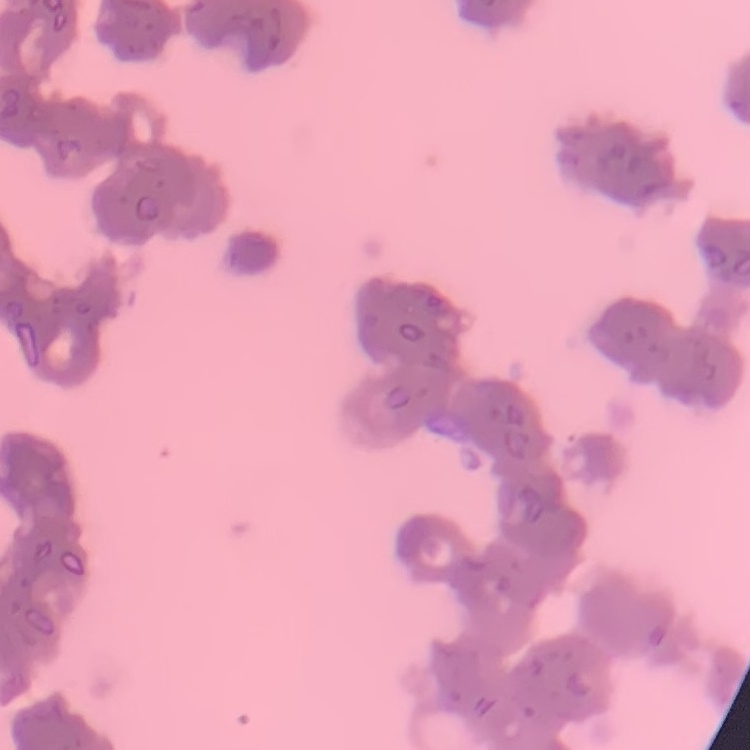
{
  "red_blood_cell_morphology": "rouleaux formation",
  "image_type": "square crop of a larger photomicrograph",
  "preparation": "thin peripheral smear",
  "stain": "Field's or Giemsa"
}